Locate every malaria parasite.
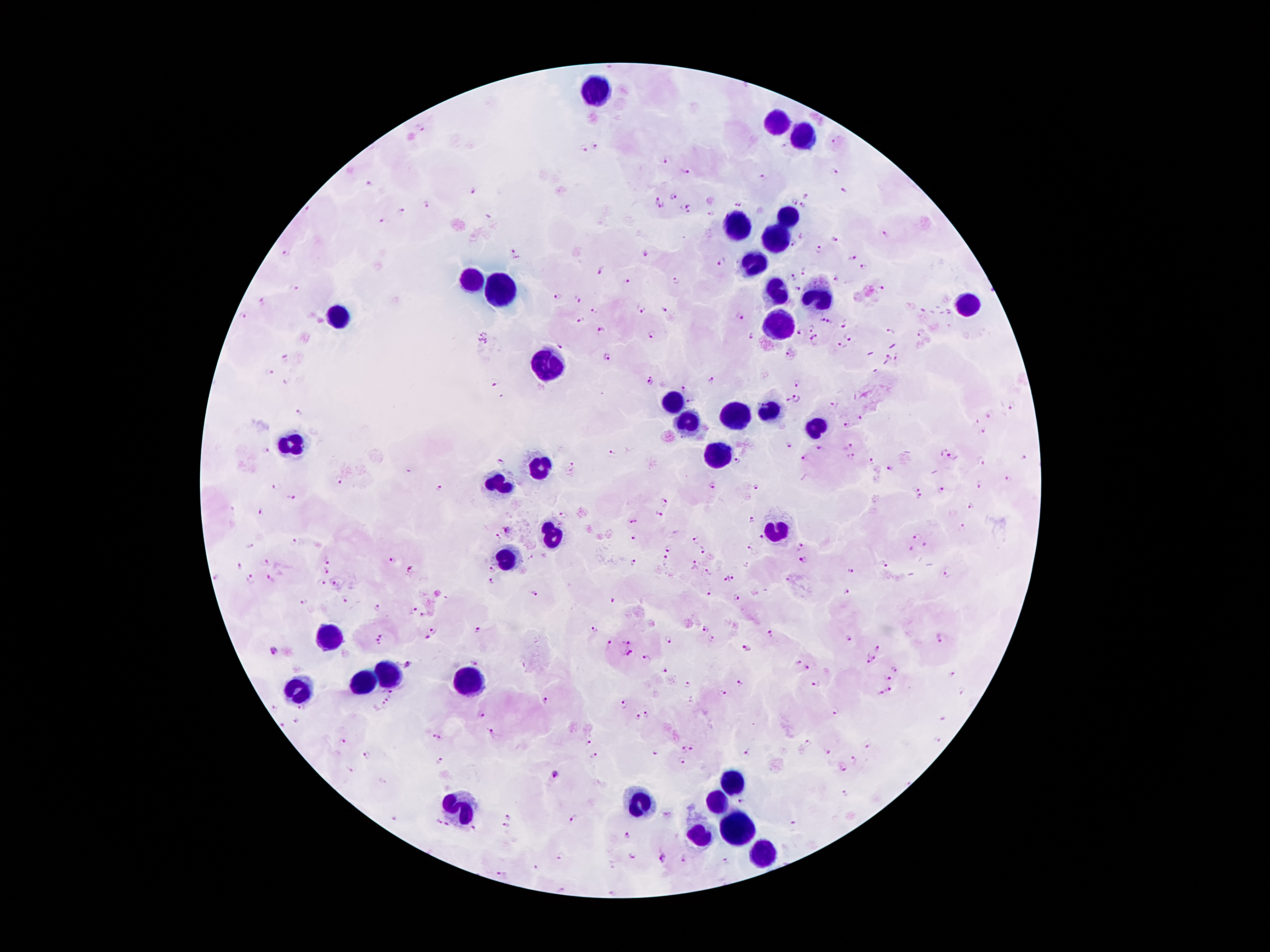
Approximate object centers, in pixels from the top-left corner.
Malaria parasites: (x=422, y=129), (x=836, y=143), (x=595, y=146), (x=784, y=146), (x=584, y=148), (x=665, y=159), (x=832, y=169), (x=684, y=172), (x=763, y=178), (x=373, y=184), (x=844, y=189), (x=472, y=190), (x=676, y=197), (x=809, y=197), (x=659, y=198), (x=795, y=201), (x=738, y=203), (x=803, y=204), (x=426, y=206), (x=662, y=208), (x=686, y=209), (x=403, y=212), (x=712, y=213), (x=490, y=216), (x=382, y=222), (x=885, y=234), (x=803, y=236), (x=836, y=240), (x=792, y=244), (x=818, y=250), (x=643, y=252), (x=515, y=256), (x=853, y=258), (x=722, y=261), (x=863, y=268), (x=600, y=271), (x=806, y=272), (x=836, y=277), (x=794, y=278), (x=676, y=280), (x=626, y=281), (x=295, y=288), (x=881, y=288), (x=797, y=289), (x=558, y=298), (x=578, y=298), (x=263, y=302), (x=639, y=309), (x=595, y=310), (x=664, y=310), (x=246, y=315), (x=740, y=316), (x=823, y=319), (x=581, y=321), (x=830, y=322), (x=845, y=322), (x=812, y=326), (x=892, y=331), (x=601, y=332), (x=800, y=332), (x=921, y=333), (x=652, y=335), (x=752, y=335), (x=849, y=338), (x=815, y=340), (x=558, y=346), (x=842, y=346), (x=887, y=356), (x=607, y=357), (x=898, y=357), (x=284, y=358), (x=271, y=373), (x=711, y=381), (x=493, y=382), (x=650, y=382), (x=800, y=383), (x=680, y=389), (x=796, y=398), (x=788, y=400), (x=691, y=401), (x=835, y=404), (x=1012, y=407), (x=298, y=412), (x=989, y=415), (x=861, y=418), (x=977, y=422), (x=846, y=424), (x=984, y=432), (x=788, y=442), (x=848, y=446), (x=817, y=448), (x=266, y=452), (x=612, y=453), (x=950, y=455), (x=805, y=457), (x=850, y=457), (x=736, y=459), (x=1022, y=459), (x=872, y=460), (x=499, y=461), (x=980, y=461), (x=572, y=466), (x=889, y=467), (x=1009, y=479), (x=340, y=480), (x=277, y=485), (x=713, y=485), (x=440, y=487), (x=756, y=487), (x=980, y=487), (x=914, y=489), (x=942, y=490), (x=292, y=496), (x=919, y=496), (x=666, y=503), (x=970, y=506), (x=261, y=512), (x=660, y=513), (x=634, y=521), (x=752, y=521), (x=962, y=527), (x=633, y=537), (x=916, y=537), (x=762, y=538), (x=698, y=539), (x=292, y=540), (x=250, y=545), (x=925, y=545), (x=801, y=547), (x=669, y=548), (x=702, y=549), (x=911, y=549), (x=751, y=550), (x=666, y=559), (x=393, y=561), (x=804, y=561), (x=327, y=562), (x=267, y=563), (x=632, y=563), (x=883, y=563), (x=697, y=564), (x=746, y=566), (x=239, y=567), (x=493, y=569), (x=410, y=570), (x=849, y=572), (x=326, y=573), (x=709, y=573), (x=946, y=574), (x=216, y=577), (x=733, y=577), (x=271, y=578), (x=250, y=579), (x=726, y=579), (x=788, y=579), (x=491, y=581), (x=335, y=582), (x=320, y=583), (x=710, y=591), (x=846, y=591), (x=535, y=593), (x=739, y=597), (x=346, y=599), (x=612, y=601), (x=305, y=602), (x=378, y=608), (x=413, y=611), (x=424, y=616), (x=593, y=629), (x=477, y=630), (x=705, y=630), (x=433, y=634), (x=771, y=634), (x=384, y=637), (x=712, y=638), (x=849, y=638), (x=939, y=639), (x=669, y=641), (x=378, y=643), (x=610, y=643), (x=626, y=643), (x=747, y=648), (x=879, y=648), (x=272, y=651), (x=628, y=653), (x=646, y=658), (x=869, y=659), (x=474, y=662), (x=798, y=663), (x=407, y=664), (x=807, y=668), (x=894, y=669), (x=666, y=672), (x=951, y=675), (x=888, y=678), (x=687, y=683), (x=741, y=683), (x=815, y=685), (x=890, y=689), (x=392, y=690), (x=960, y=691), (x=881, y=693), (x=721, y=694), (x=388, y=698), (x=546, y=701), (x=623, y=705), (x=383, y=707), (x=275, y=708), (x=303, y=708), (x=835, y=710), (x=483, y=715), (x=646, y=715), (x=637, y=717), (x=942, y=719), (x=294, y=722), (x=282, y=726), (x=493, y=733), (x=435, y=736), (x=343, y=741), (x=936, y=741), (x=590, y=742), (x=807, y=743), (x=868, y=744), (x=693, y=749), (x=683, y=750), (x=747, y=753), (x=655, y=754), (x=828, y=754), (x=366, y=755), (x=595, y=757), (x=855, y=759), (x=682, y=761), (x=441, y=762), (x=843, y=767), (x=555, y=775), (x=845, y=793), (x=741, y=800), (x=508, y=816), (x=573, y=817), (x=395, y=821), (x=439, y=823), (x=448, y=825), (x=791, y=825), (x=507, y=827), (x=473, y=828), (x=628, y=838), (x=560, y=856), (x=631, y=856), (x=663, y=859), (x=685, y=860), (x=727, y=862), (x=533, y=867), (x=501, y=876).

{
  "image_size": "1270×952 pixels",
  "field_of_view": "one from this slide",
  "stain": "Giemsa",
  "preparation": "thick blood film",
  "capture": "smartphone camera through the microscope eyepiece",
  "patient_malaria_status": "infected with Plasmodium falciparum",
  "leukocyte_locations": "approximate object centers, in pixels from the top-left corner: (x=595, y=94), (x=775, y=126), (x=803, y=136), (x=786, y=218), (x=734, y=228), (x=773, y=240), (x=758, y=266), (x=477, y=281), (x=500, y=290), (x=773, y=292), (x=816, y=299), (x=968, y=304), (x=337, y=314), (x=776, y=327), (x=543, y=368), (x=673, y=406), (x=768, y=413), (x=737, y=416), (x=688, y=427), (x=811, y=429), (x=290, y=443), (x=717, y=460), (x=539, y=469), (x=501, y=487), (x=770, y=531), (x=551, y=536), (x=508, y=565), (x=332, y=640), (x=383, y=679), (x=467, y=683), (x=361, y=688), (x=295, y=691), (x=732, y=781), (x=638, y=803), (x=716, y=805), (x=462, y=810), (x=739, y=832), (x=699, y=839), (x=758, y=853)",
  "magnification": "100x"
}